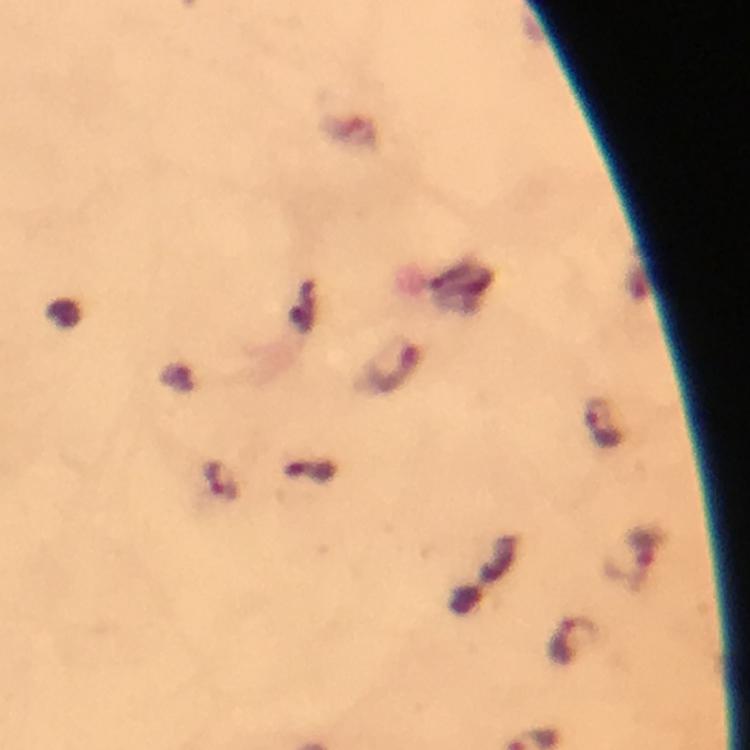
Approximate centers as [x, y] in pixels. Malaria parasite locations: [603, 425], [219, 483], [636, 557], [573, 640]. At 100x magnification. Giemsa-stained preparation. Photographed with a smartphone mounted on the microscope. Thick smear. Cropped region of a single field of view. Image is 750×750 pixels. Immersion oil applied. From a malaria diagnostic workup.